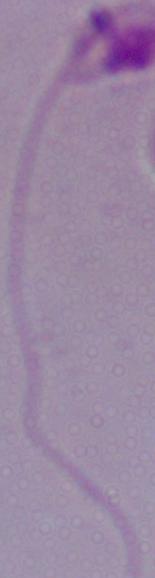
Summary:
  - Modality: micrograph
  - Magnification: 1000x
  - Identification: Leishmania